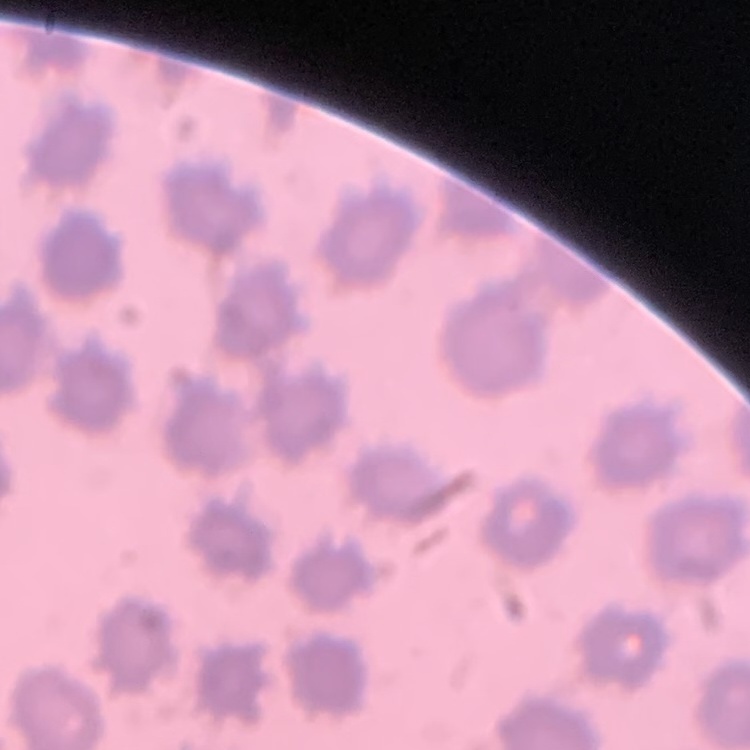

The red blood cells show no rouleaux formation. Thin peripheral smear. Square crop of a larger photomicrograph. Field's or Giemsa stain.